Give the extent of all Plasmodium falciparum-infected red blood cells.
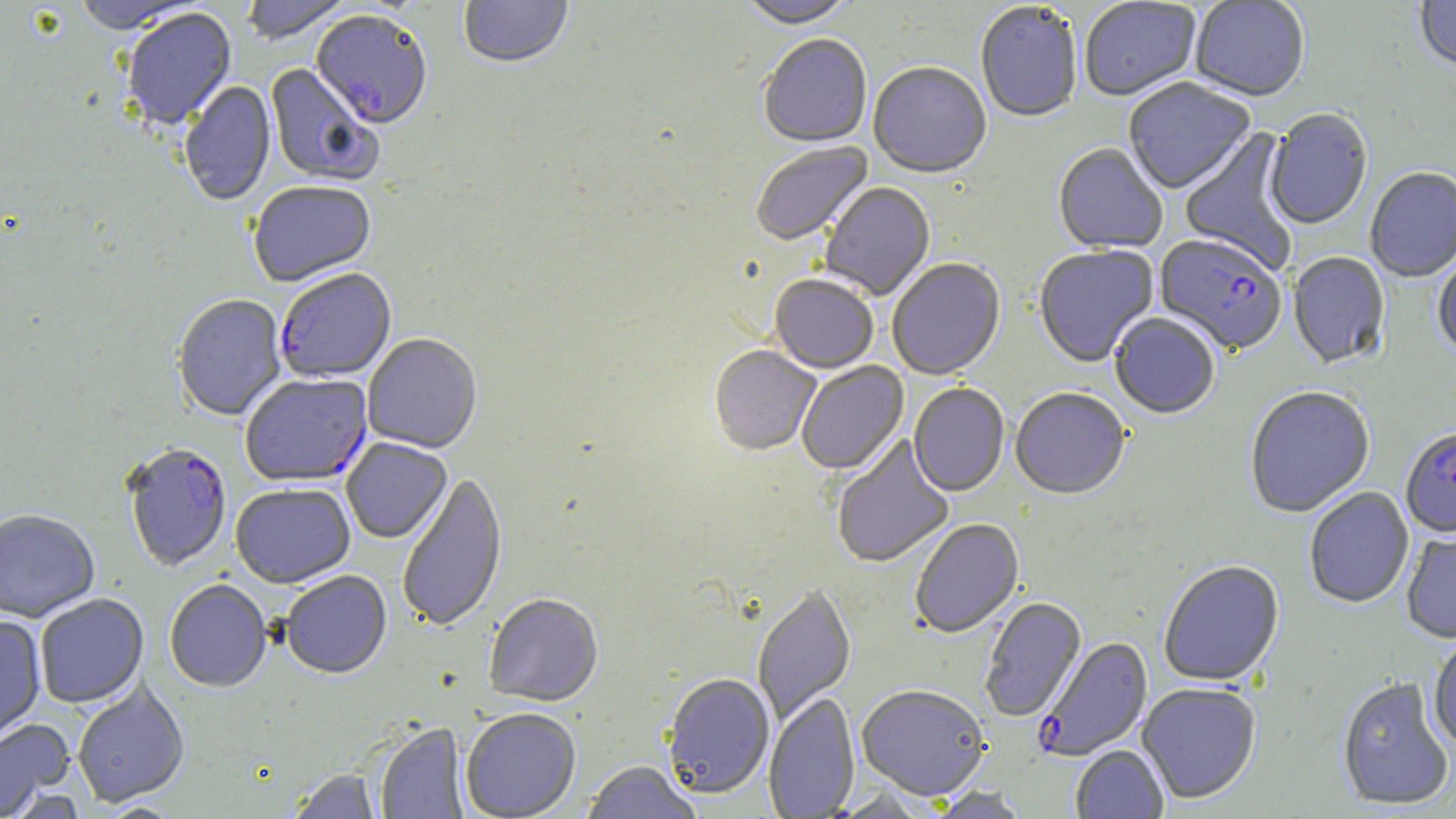

Approximate bounding boxes as named x1/y1/x2/y2 corners in pixels.
Plasmodium falciparum-infected red blood cells: (x1=310, y1=13, x2=433, y2=131), (x1=1154, y1=235, x2=1288, y2=357), (x1=275, y1=270, x2=397, y2=384), (x1=240, y1=375, x2=372, y2=488), (x1=1400, y1=429, x2=1456, y2=538), (x1=121, y1=444, x2=232, y2=573), (x1=1035, y1=637, x2=1153, y2=761).

Uninfected red blood cell locations: (x1=241, y1=0, x2=353, y2=47), (x1=459, y1=0, x2=573, y2=71), (x1=1079, y1=0, x2=1202, y2=103), (x1=1190, y1=0, x2=1310, y2=104), (x1=1414, y1=0, x2=1456, y2=73), (x1=72, y1=1, x2=202, y2=37), (x1=737, y1=1, x2=859, y2=32), (x1=975, y1=3, x2=1083, y2=125), (x1=122, y1=9, x2=237, y2=132), (x1=757, y1=36, x2=872, y2=149), (x1=265, y1=64, x2=382, y2=187), (x1=868, y1=64, x2=991, y2=180), (x1=1123, y1=79, x2=1256, y2=196), (x1=180, y1=82, x2=276, y2=207), (x1=1264, y1=109, x2=1373, y2=231), (x1=1179, y1=127, x2=1300, y2=275), (x1=750, y1=143, x2=875, y2=248), (x1=1053, y1=144, x2=1168, y2=255), (x1=1365, y1=168, x2=1456, y2=283), (x1=820, y1=182, x2=936, y2=301), (x1=248, y1=183, x2=377, y2=289), (x1=1034, y1=246, x2=1159, y2=368), (x1=1288, y1=253, x2=1391, y2=370), (x1=1432, y1=256, x2=1456, y2=357), (x1=887, y1=259, x2=1006, y2=382), (x1=769, y1=276, x2=878, y2=375), (x1=172, y1=295, x2=287, y2=422), (x1=1109, y1=314, x2=1220, y2=421), (x1=362, y1=334, x2=482, y2=454), (x1=708, y1=347, x2=820, y2=457), (x1=796, y1=362, x2=910, y2=476), (x1=908, y1=384, x2=1009, y2=498), (x1=1246, y1=387, x2=1375, y2=519), (x1=1010, y1=389, x2=1130, y2=501), (x1=831, y1=436, x2=955, y2=569), (x1=341, y1=438, x2=452, y2=544), (x1=396, y1=471, x2=508, y2=634), (x1=231, y1=484, x2=356, y2=589), (x1=1304, y1=488, x2=1414, y2=609), (x1=0, y1=510, x2=100, y2=623), (x1=910, y1=519, x2=1025, y2=639), (x1=1401, y1=531, x2=1456, y2=645), (x1=1159, y1=561, x2=1284, y2=688), (x1=281, y1=571, x2=392, y2=680), (x1=164, y1=580, x2=272, y2=694), (x1=753, y1=586, x2=857, y2=727), (x1=35, y1=594, x2=149, y2=709), (x1=484, y1=595, x2=604, y2=707), (x1=980, y1=598, x2=1087, y2=722), (x1=0, y1=617, x2=46, y2=742), (x1=1428, y1=635, x2=1456, y2=753), (x1=662, y1=675, x2=775, y2=801), (x1=1337, y1=678, x2=1454, y2=811), (x1=72, y1=681, x2=190, y2=808), (x1=1137, y1=683, x2=1261, y2=804), (x1=856, y1=686, x2=990, y2=801), (x1=764, y1=693, x2=860, y2=818), (x1=461, y1=709, x2=581, y2=819), (x1=0, y1=718, x2=75, y2=818), (x1=375, y1=723, x2=469, y2=818), (x1=1071, y1=745, x2=1168, y2=819), (x1=580, y1=762, x2=704, y2=819), (x1=287, y1=769, x2=382, y2=819), (x1=927, y1=787, x2=1031, y2=818). Slide-level diagnosis: Plasmodium falciparum. Optical microscopy. May-Grünwald-Giemsa-stained preparation. Thin blood smear. Image is 1456×819 pixels. One field of a larger specimen. 1000x magnification.